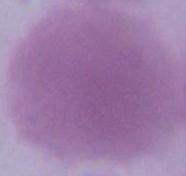

magnification = 1000x
modality = micrograph
identification = erythrocyte